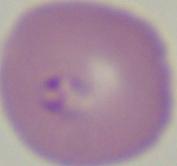
Summary:
  - Magnification: 1000x
  - Modality: micrograph
  - Identification: Babesia